Give a bounding box for every parasitised red blood cell.
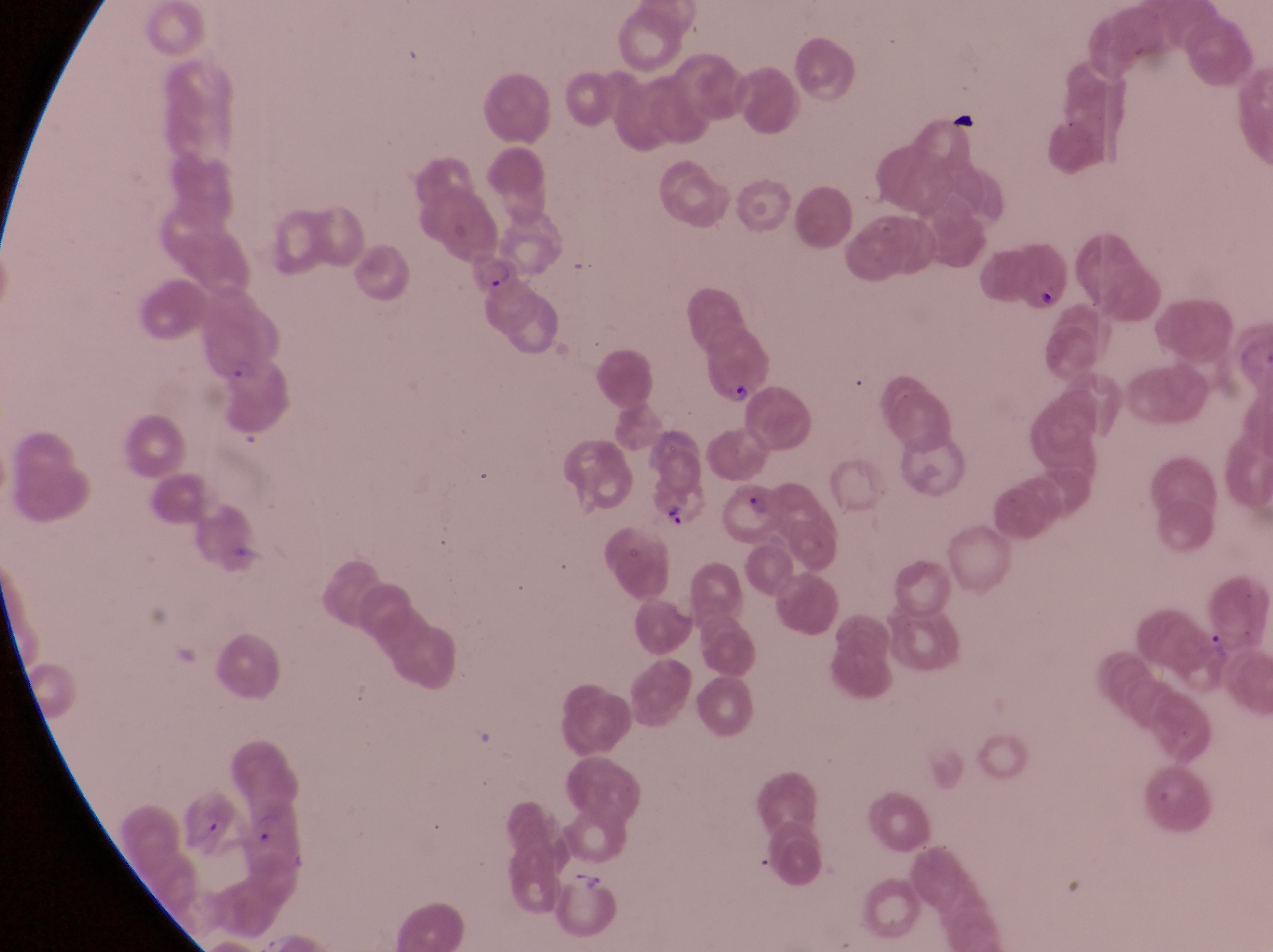

Approximate bounding boxes as (left, top, right, bottom) in pixels.
Parasitised red blood cells: (462, 244, 520, 297), (694, 320, 771, 407), (647, 472, 709, 534), (716, 484, 790, 546).

Summary:
  - Artifact (platelet-like body, stain precipitate, or debris) locations: (1031, 282, 1059, 309)
  - Country: Uganda
  - Preparation: thin blood film
  - Image size: 1273×952 pixels
  - Capture: smartphone photograph through the eyepiece of an Olympus CX-23 microscope
  - Magnification: 1000x
  - Field of view: single